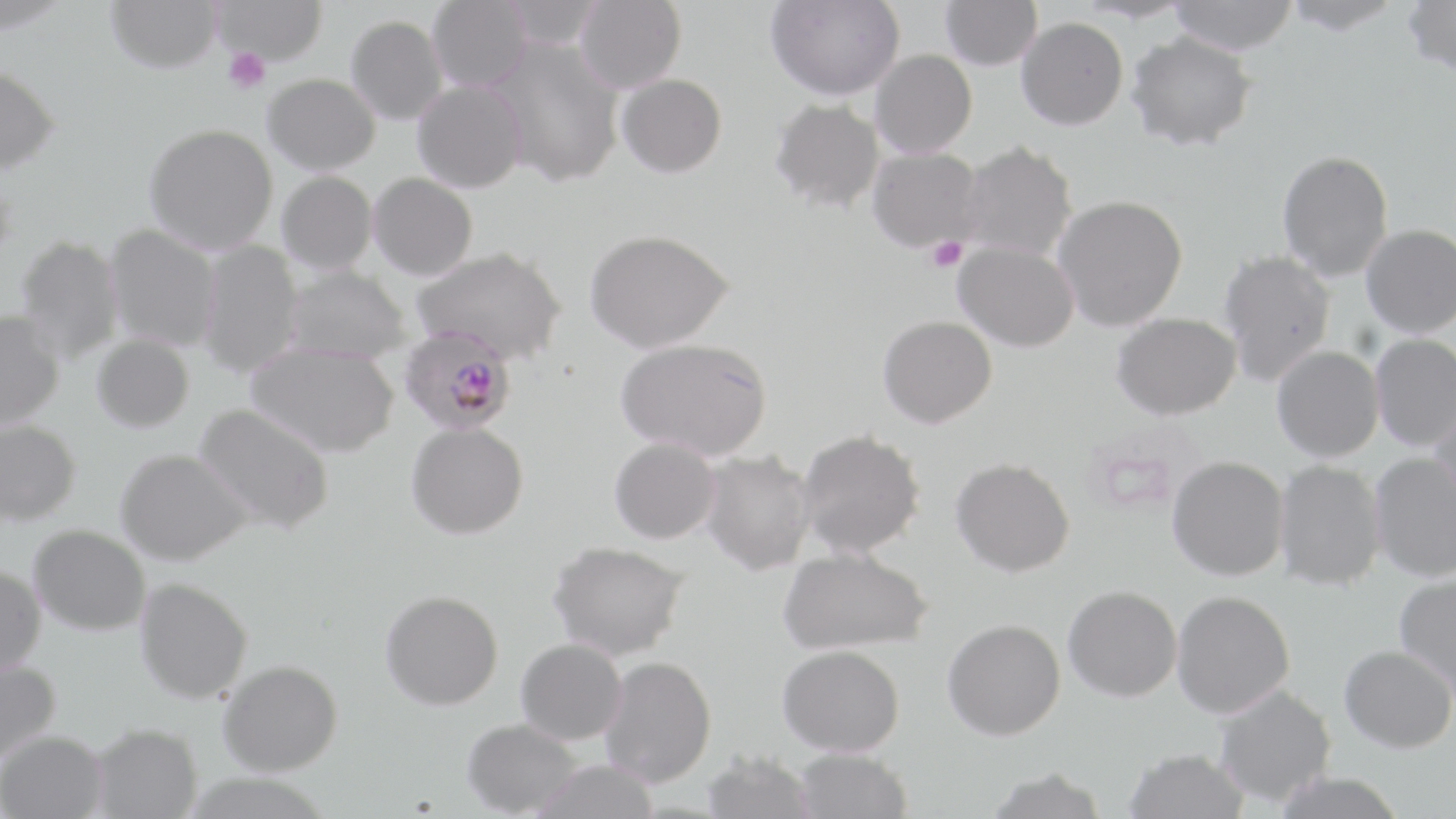

Approximate bounding boxes as [x1, y1, x2, y2] in pixels. Platelet locations: [222, 47, 271, 95], [928, 237, 968, 272]. Plasmodium falciparum-infected red blood cell locations: [399, 328, 517, 435]. Uninfected red blood cell locations: [105, 0, 221, 76], [212, 0, 328, 67], [427, 0, 533, 93], [574, 0, 686, 94], [765, 0, 904, 102], [940, 0, 1042, 71], [1073, 0, 1194, 24], [1169, 0, 1298, 56], [1281, 0, 1405, 35], [1402, 0, 1456, 78], [501, 1, 607, 50], [346, 16, 448, 125], [1016, 17, 1127, 130], [1126, 32, 1257, 152], [488, 38, 625, 188], [871, 50, 976, 158], [0, 68, 60, 178], [617, 74, 726, 180], [264, 75, 380, 175], [412, 80, 527, 194], [769, 98, 884, 213], [144, 125, 278, 255], [958, 143, 1077, 261], [868, 147, 984, 252], [1277, 150, 1394, 282], [277, 171, 377, 274], [368, 173, 478, 281], [1053, 196, 1187, 331], [1361, 224, 1456, 338], [104, 225, 221, 351], [585, 229, 734, 353], [14, 236, 124, 364], [197, 240, 304, 378], [953, 242, 1079, 352], [413, 247, 568, 365], [1218, 250, 1336, 386], [283, 266, 410, 364], [0, 312, 64, 430], [1111, 313, 1241, 420], [878, 316, 996, 428], [1370, 333, 1456, 452], [92, 335, 194, 433], [616, 337, 772, 460], [245, 342, 399, 458], [1272, 346, 1383, 462], [1430, 396, 1456, 514], [194, 403, 335, 534], [0, 420, 82, 525], [406, 422, 528, 539], [796, 429, 925, 558], [609, 437, 720, 544], [115, 448, 252, 565], [700, 450, 815, 575], [1369, 453, 1456, 582], [1167, 456, 1288, 581], [950, 457, 1075, 577], [1274, 460, 1386, 591], [29, 524, 150, 635], [548, 540, 688, 661], [778, 547, 932, 655], [0, 567, 46, 677], [1393, 574, 1456, 701], [135, 578, 253, 704], [1063, 585, 1182, 701], [380, 590, 503, 710], [1171, 590, 1294, 718], [942, 619, 1066, 740], [516, 638, 626, 745], [778, 645, 905, 755], [1339, 645, 1456, 753], [600, 656, 717, 788], [0, 659, 61, 765], [218, 659, 343, 775], [1215, 685, 1336, 807], [462, 718, 581, 817], [91, 723, 202, 818], [0, 730, 108, 819], [1123, 747, 1251, 819], [793, 748, 912, 819], [701, 751, 819, 819], [530, 759, 659, 819], [984, 767, 1109, 819], [1270, 772, 1407, 819]. Slide-level diagnosis: Plasmodium falciparum. Image is 1456×819 pixels. 1000x magnification. Thin blood film. May-Grünwald-Giemsa stain. Single field of view. Light microscopy.